Identify the parasite.
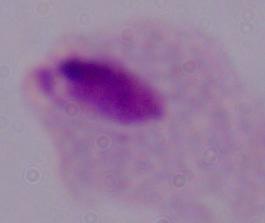

A trichomonad.

Micrograph. Captured at 1000x magnification.